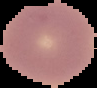
image type = cell region segmented out of the field of view; surrounding area masked to black
preparation = thin blood film
image size = 97×88 pixels
result = no Plasmodium parasites seen